Locate every uninfected red blood cell.
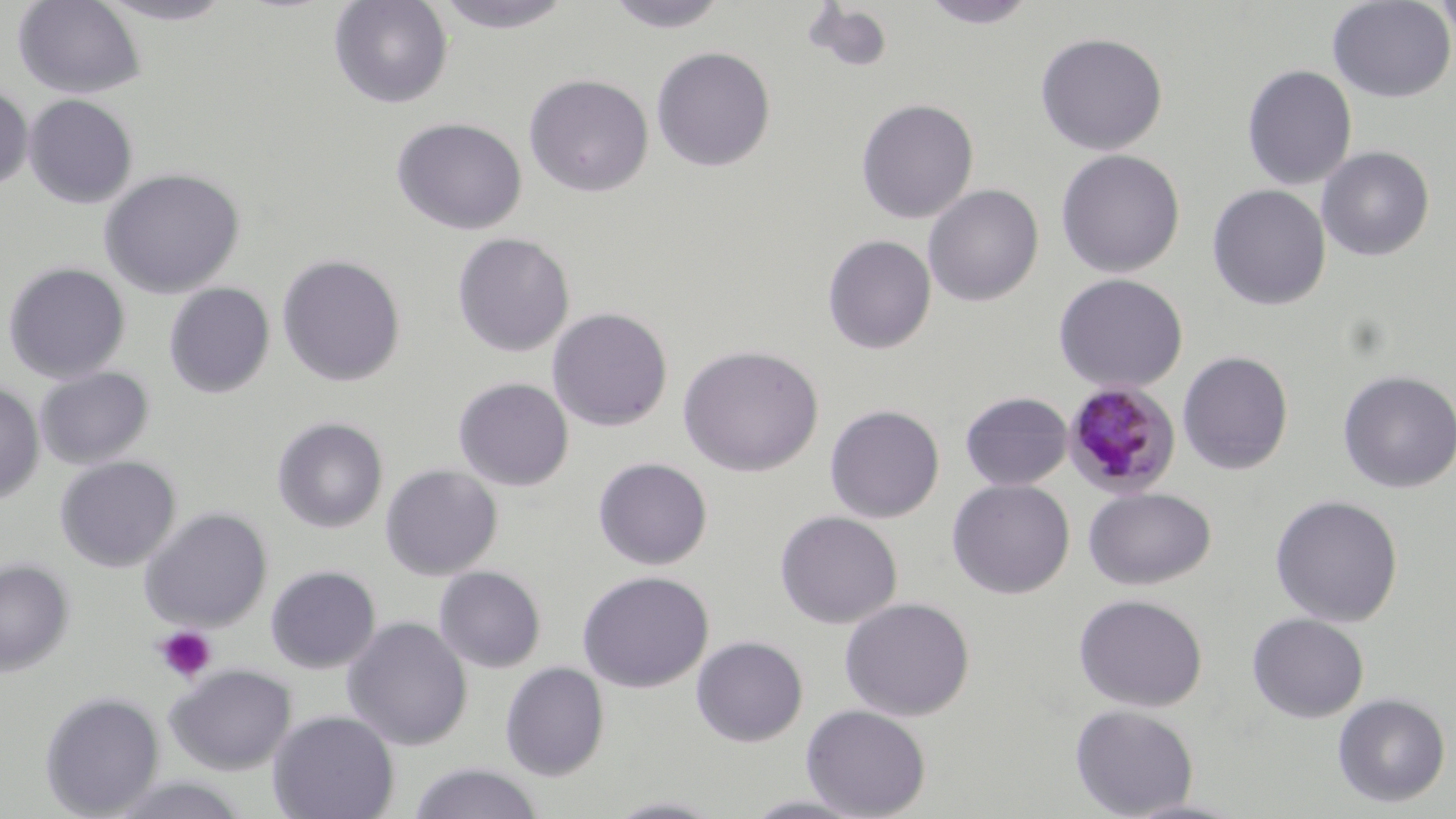

Approximate bounding boxes as [x1, y1, x2, y2] in pixels.
Uninfected red blood cells: [13, 0, 146, 99], [94, 0, 238, 25], [328, 0, 454, 109], [604, 0, 731, 33], [919, 0, 1040, 28], [1327, 0, 1456, 103], [1434, 0, 1456, 49], [431, 1, 579, 34], [803, 3, 894, 73], [1035, 31, 1168, 155], [651, 46, 776, 172], [1242, 64, 1357, 190], [523, 74, 654, 197], [0, 85, 33, 192], [24, 94, 138, 208], [856, 98, 979, 223], [390, 116, 527, 235], [1316, 145, 1435, 261], [1055, 149, 1185, 278], [98, 167, 246, 299], [923, 184, 1043, 307], [1207, 184, 1331, 310], [452, 232, 575, 357], [822, 234, 936, 354], [276, 254, 407, 387], [2, 261, 131, 384], [1053, 272, 1188, 393], [164, 282, 276, 398], [547, 307, 673, 431], [677, 344, 824, 477], [1177, 351, 1294, 475], [35, 366, 154, 469], [1337, 370, 1456, 494], [453, 377, 574, 491], [0, 381, 44, 505], [960, 391, 1073, 491], [825, 404, 945, 523], [272, 416, 389, 533], [55, 456, 180, 572], [593, 457, 713, 570], [380, 464, 502, 580], [947, 479, 1075, 599], [1084, 486, 1217, 591], [1270, 495, 1404, 627], [139, 507, 273, 632], [774, 510, 902, 629], [0, 558, 75, 676], [265, 565, 381, 674], [434, 566, 546, 673], [577, 570, 714, 693], [1073, 593, 1208, 712], [839, 596, 975, 721], [1247, 613, 1369, 723], [342, 616, 473, 751], [691, 636, 808, 747], [499, 662, 610, 782], [165, 663, 296, 775], [40, 691, 165, 818], [1332, 692, 1451, 808], [801, 704, 932, 818], [1070, 704, 1199, 818], [268, 710, 400, 819], [408, 762, 544, 819], [103, 775, 253, 819], [739, 793, 875, 817], [602, 796, 728, 818].

Plasmodium malariae-infected red blood cell locations: [1062, 380, 1181, 499]. Platelet locations: [154, 626, 217, 683]. Slide-level diagnosis: Plasmodium malariae. Single field of view. Light microscopy. Captured at 1000x magnification. May-Grünwald-Giemsa-stained preparation. Image is 1456×819 pixels. Thin blood film.